Describe the morphology of the erythrocytes.
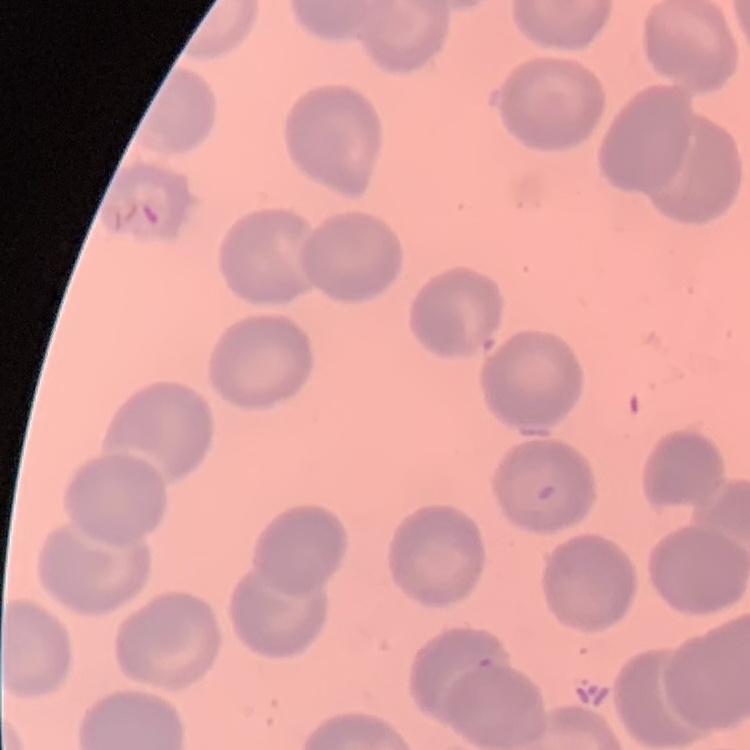

They show no rouleaux formation.

Summary:
  - Preparation: thin blood smear
  - Stain: Field's or Giemsa
  - Image type: square crop of a larger photomicrograph